Give the position of every Plasmodium parasite.
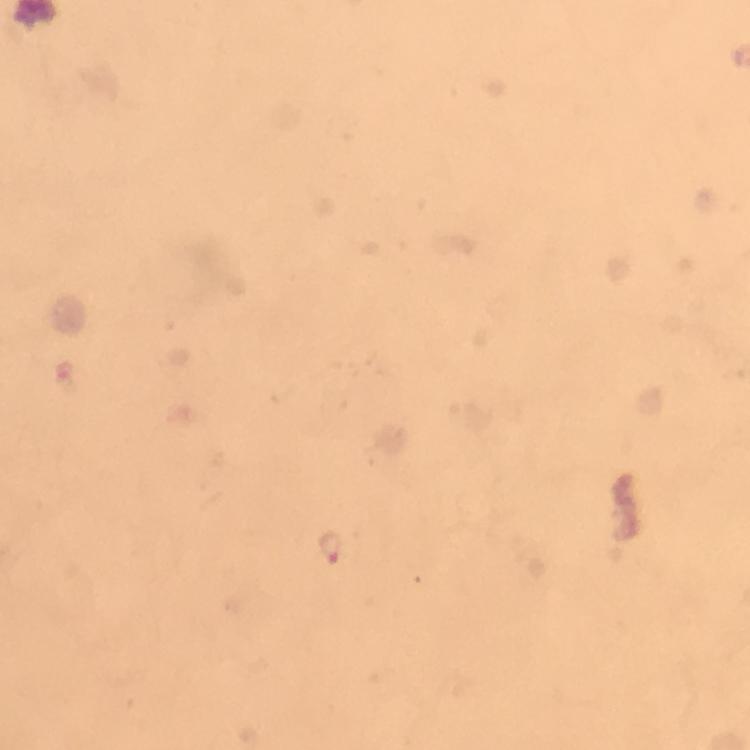
Approximate centers as [x, y] in pixels.
Plasmodium parasites: [67, 377], [329, 548].

image_size: 750×750 pixels
stain: Giemsa
cropped_from: a single field of view
immersion_oil: applied
preparation: thick smear
context: from a malaria diagnostic workup
magnification: 100x
capture: smartphone mounted on the microscope